Locate every malaria parasite and every leukocyte.
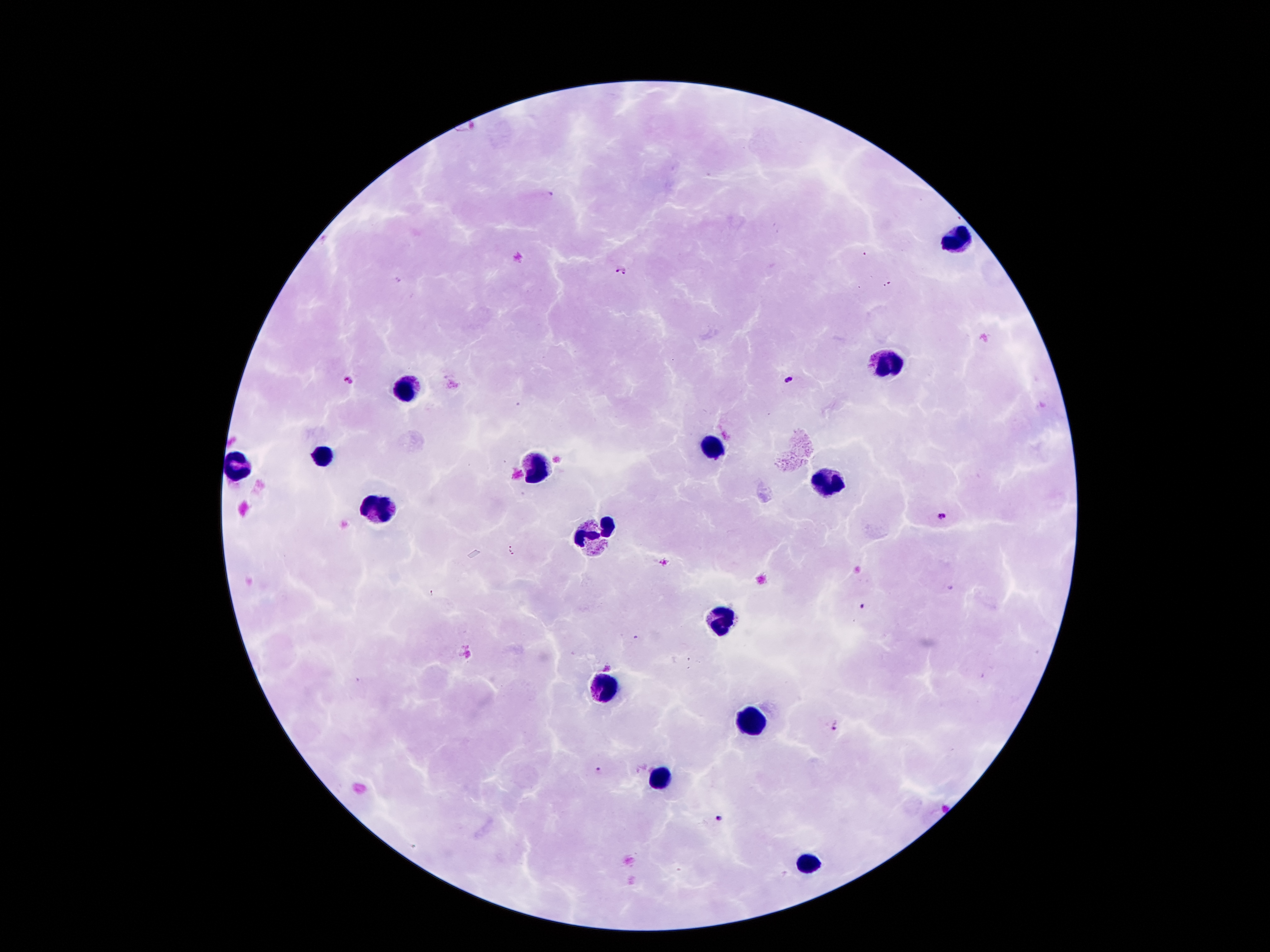

Approximate centers as (x, y) in pixels.
Malaria parasites: (466, 136), (621, 271), (346, 381), (789, 381), (942, 515), (510, 551), (863, 608), (834, 726), (597, 769), (720, 818).
Leukocytes: (957, 237), (889, 361), (407, 387), (713, 450), (321, 456), (237, 468), (539, 470), (829, 483), (377, 510), (595, 533), (719, 618), (604, 685), (745, 722), (661, 779), (805, 863).

stain = Giemsa
magnification = 100x
patient malaria status = infected with Plasmodium falciparum
image size = 1270×952 pixels
capture = smartphone through the microscope eyepiece
preparation = thick blood film
field of view = one from this slide